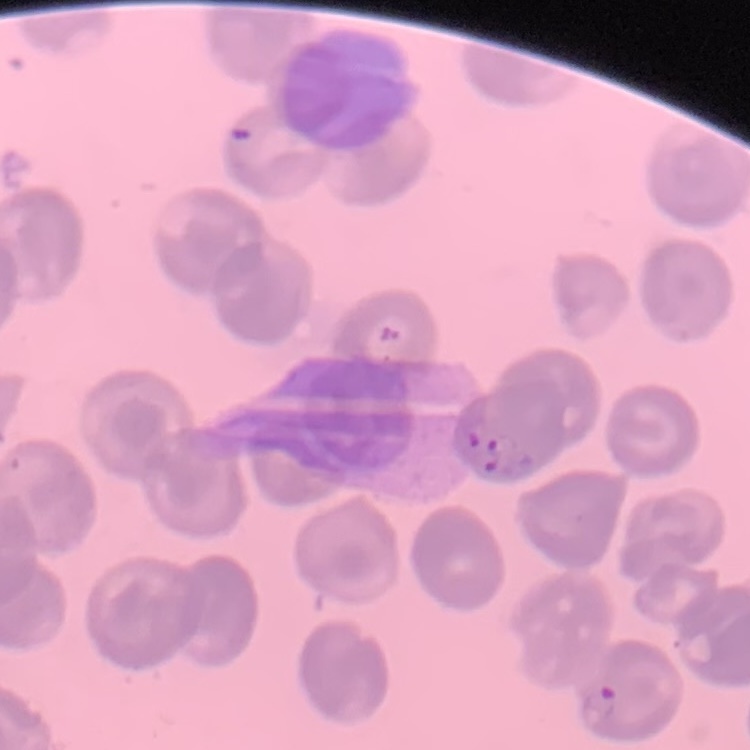 The erythrocytes exhibit no rouleaux formation. Thin blood film. Stained with either Field's or Giemsa. Square crop of a larger photomicrograph.